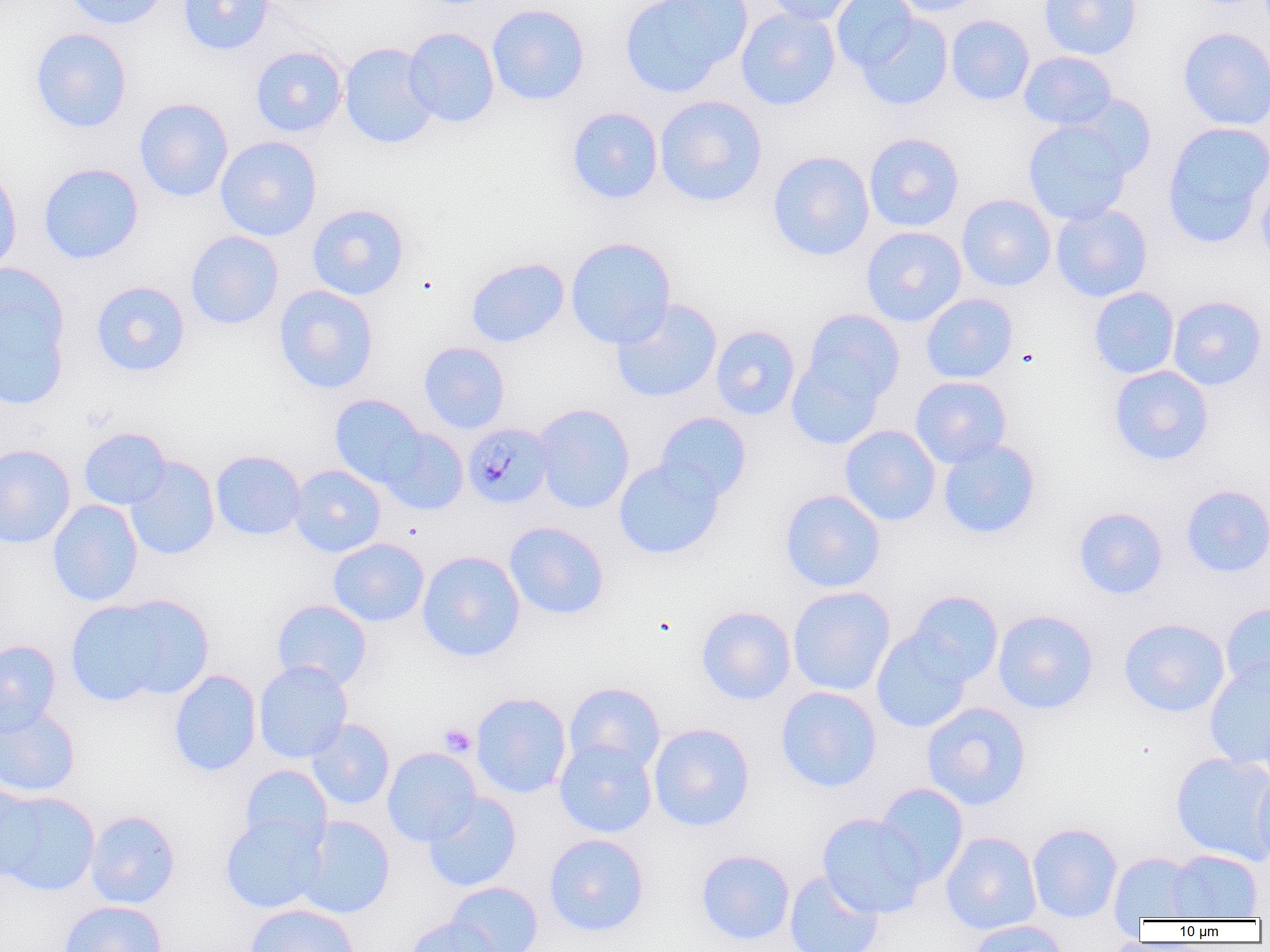
slide-level diagnosis = Plasmodium malariae
image size = 1270×952 pixels
platelet locations = approximate bounding boxes as (x1, y1, x2, y2) in pixels: (439, 722, 477, 757)
uninfected red blood cell locations = approximate bounding boxes as (x1, y1, x2, y2) in pixels: (63, 0, 169, 30), (177, 0, 276, 55), (619, 0, 750, 98), (763, 0, 864, 26), (831, 0, 920, 72), (887, 0, 989, 17), (1038, 0, 1142, 60), (487, 3, 590, 106), (735, 7, 841, 111), (853, 12, 953, 110), (945, 14, 1035, 106), (30, 27, 132, 133), (403, 27, 500, 128), (1177, 27, 1270, 130), (339, 43, 440, 149), (249, 45, 348, 137), (1018, 51, 1118, 130), (1063, 94, 1157, 180), (654, 95, 768, 207), (134, 98, 233, 202), (566, 106, 664, 204), (1023, 119, 1134, 226), (1161, 121, 1270, 248), (864, 132, 964, 232), (215, 136, 321, 241), (767, 150, 875, 261), (0, 161, 22, 276), (38, 162, 144, 265), (1255, 168, 1270, 274), (957, 194, 1056, 292), (1050, 203, 1153, 302), (307, 204, 409, 300), (860, 226, 967, 327), (185, 230, 284, 330), (565, 236, 676, 348), (465, 257, 569, 347), (0, 261, 70, 379), (90, 280, 190, 377), (274, 285, 378, 394), (1088, 287, 1179, 379), (920, 293, 1017, 384), (1167, 295, 1267, 390), (611, 298, 722, 403), (801, 308, 905, 408), (709, 323, 902, 413), (710, 325, 800, 420), (418, 341, 510, 434), (786, 352, 888, 450), (1108, 365, 1214, 465), (910, 376, 1012, 468), (329, 393, 427, 488), (532, 403, 635, 514), (654, 411, 751, 503), (840, 425, 941, 526), (78, 427, 172, 510), (378, 428, 468, 515), (937, 438, 1042, 540), (0, 444, 75, 549), (210, 450, 306, 540), (613, 457, 725, 560), (125, 458, 220, 560), (288, 464, 387, 557), (1180, 484, 1270, 577), (780, 489, 885, 592), (47, 500, 143, 606), (1073, 507, 1168, 600), (504, 521, 609, 620), (328, 537, 429, 627), (417, 550, 526, 662), (787, 586, 895, 696), (906, 591, 1003, 686), (66, 594, 212, 706), (271, 599, 372, 690), (1220, 601, 1270, 693), (696, 606, 796, 704), (992, 610, 1098, 714), (1119, 617, 1230, 717), (871, 628, 974, 733), (0, 640, 61, 735), (1204, 657, 1270, 769), (253, 661, 353, 763), (168, 669, 262, 776), (564, 682, 666, 775), (775, 686, 882, 792), (471, 692, 572, 799), (921, 702, 1032, 810), (0, 704, 81, 798), (306, 719, 395, 809), (648, 723, 755, 832), (554, 738, 657, 838), (382, 747, 482, 846), (1170, 750, 1270, 865), (240, 765, 332, 850), (1251, 769, 1270, 871), (875, 783, 969, 887), (0, 785, 43, 883), (1, 790, 100, 895), (423, 793, 522, 892), (85, 810, 180, 908), (220, 813, 328, 913), (817, 813, 928, 918), (294, 815, 396, 918), (1027, 822, 1123, 923), (941, 831, 1042, 935), (544, 833, 649, 937), (695, 849, 795, 945), (1166, 849, 1263, 919), (1108, 852, 1201, 922), (784, 870, 884, 952), (446, 881, 543, 952), (59, 900, 167, 952), (244, 904, 360, 952), (405, 916, 500, 952), (967, 920, 1070, 952)
preparation = thin blood smear
Plasmodium malariae-infected red blood cell locations = approximate bounding boxes as (x1, y1, x2, y2) in pixels: (462, 423, 554, 509)
field of view = one of a larger specimen
modality = light microscopy
magnification = 1000x